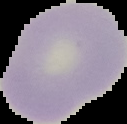 From a thin blood smear. Result: no malaria parasites seen. Segmented cell region on a black background. Image is 127×124 pixels.